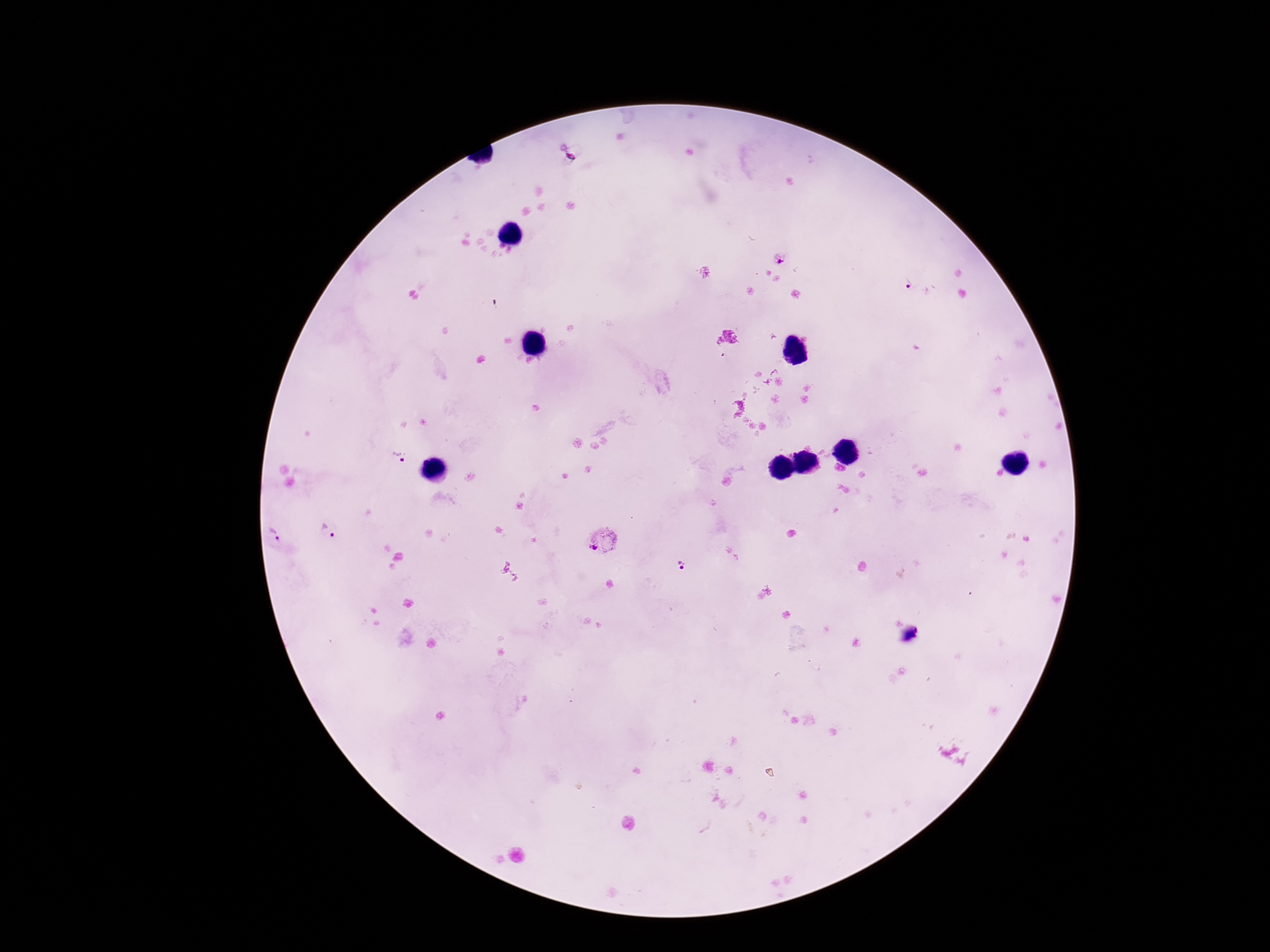

Approximate centers as [x, y] in pixels. Plasmodium parasite locations: [569, 152], [779, 256], [909, 285], [400, 456], [328, 530], [273, 535], [604, 543], [679, 564]. Thick peripheral-blood smear. Giemsa stain. Patient malaria status: infected. 100x magnification. Image is 1270×952 pixels. One field from this slide. Photographed through the microscope eyepiece with a smartphone camera.